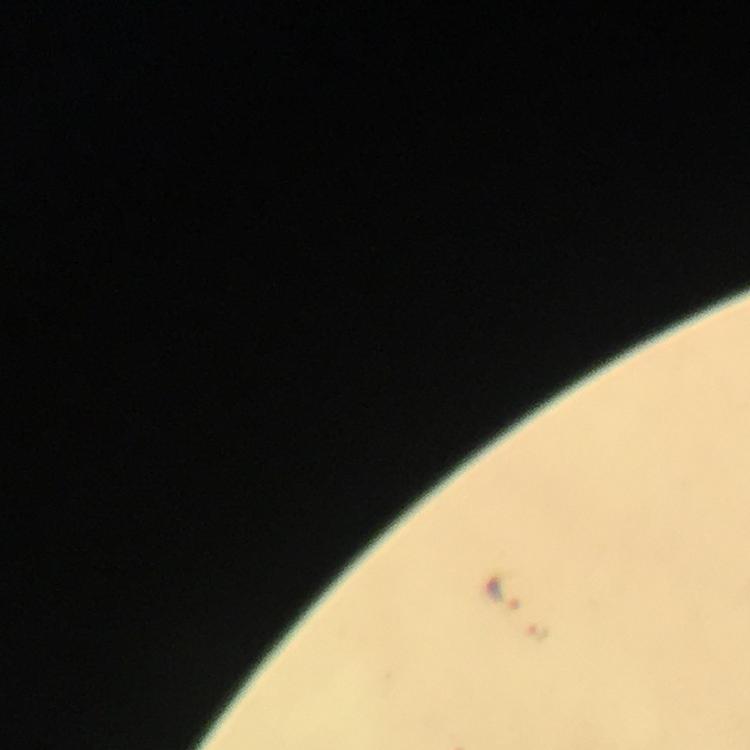
Approximate centers as {x, y} in pixels. Malaria parasite locations: {505, 590}, {536, 633}. Giemsa-stained preparation. Thick blood smear. A crop from one field of view. From a diagnostic examination for malaria. Immersion oil was used. At 100x magnification. Photographed with a smartphone mounted on the microscope. Image is 750×750 pixels.